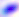
identification = Toxoplasma gondii
modality = photomicrograph
magnification = 400x